Assess the background quality.
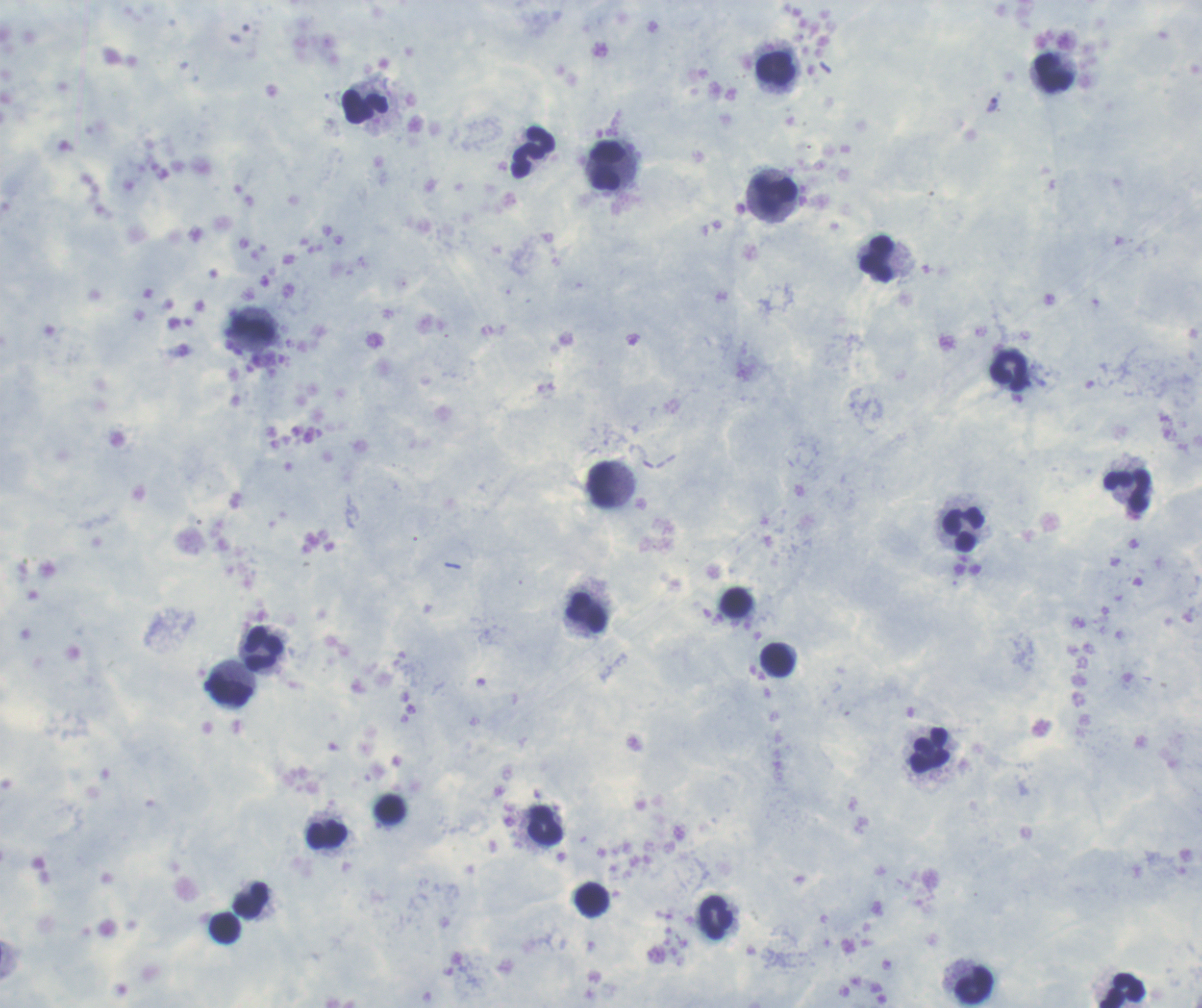

It is good.

coordinate format = approximate centers as (x, y) in pixels
trophozoite locations = (993, 105)
leukocyte locations = (776, 68), (1054, 72), (365, 106), (533, 152), (608, 165), (774, 195), (877, 259), (253, 330), (1010, 370), (601, 485), (1127, 492), (964, 530), (735, 602), (586, 612), (263, 647), (777, 660), (229, 689), (929, 750), (545, 825), (326, 834), (592, 900), (252, 901), (715, 919), (224, 928), (973, 985), (1122, 990)
result = Plasmodium parasites detected
image size = 1202×1008 pixels
preparation = thick blood smear
context = previously used in an actual diagnosis
field of view = one from this slide
magnification = 100x
stain = Romanowsky
coloration quality = good